State which parasite is depicted.
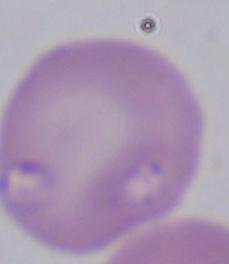
This is Babesia.

magnification = 1000x
modality = micrograph